Describe the morphology of the erythrocytes.
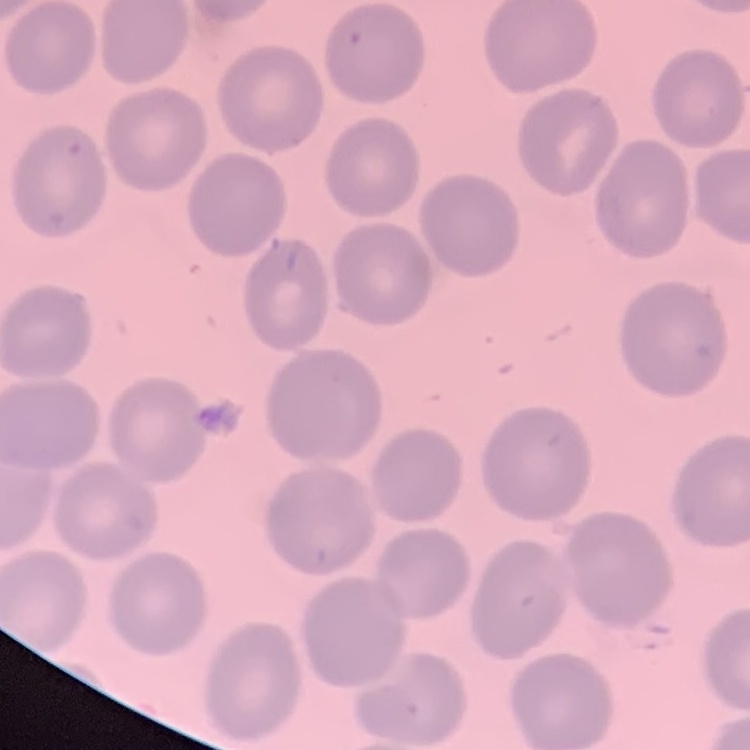
They show no rouleaux formation.

preparation: thin blood film
image_type: square crop of a larger photomicrograph
stain: Field's or Giemsa